Assess the morphology of the erythrocytes.
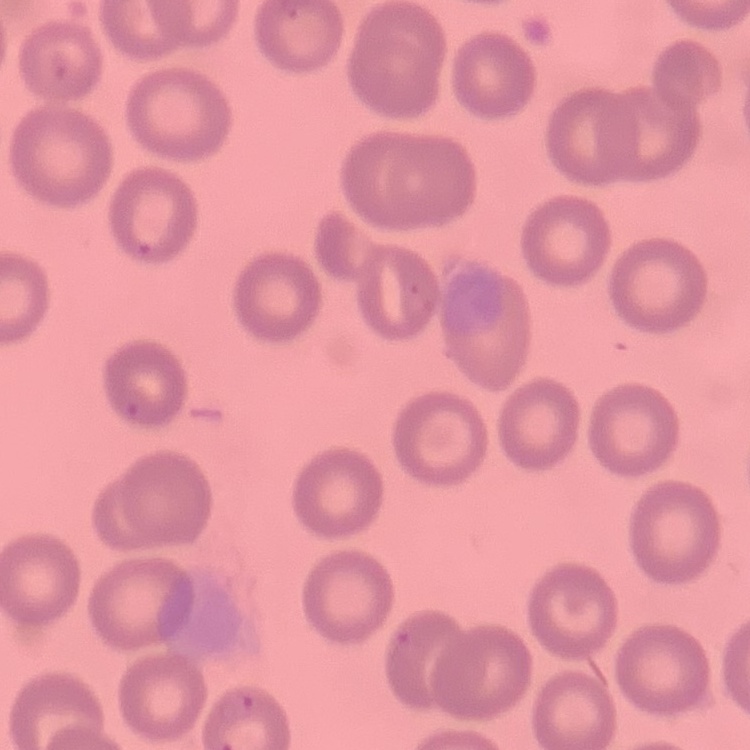
They show no rouleaux formation.

Summary:
  - Stain: Field's or Giemsa
  - Preparation: thin blood smear
  - Image type: square crop of a larger photomicrograph